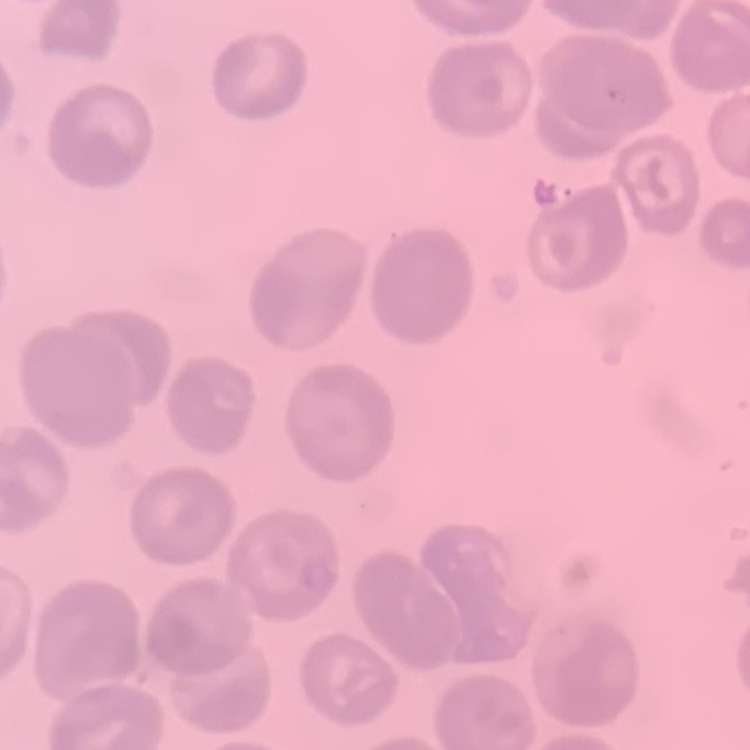
The erythrocytes exhibit no rouleaux formation. Stained with either Field's or Giemsa. Thin blood film. Square crop of a larger photomicrograph.